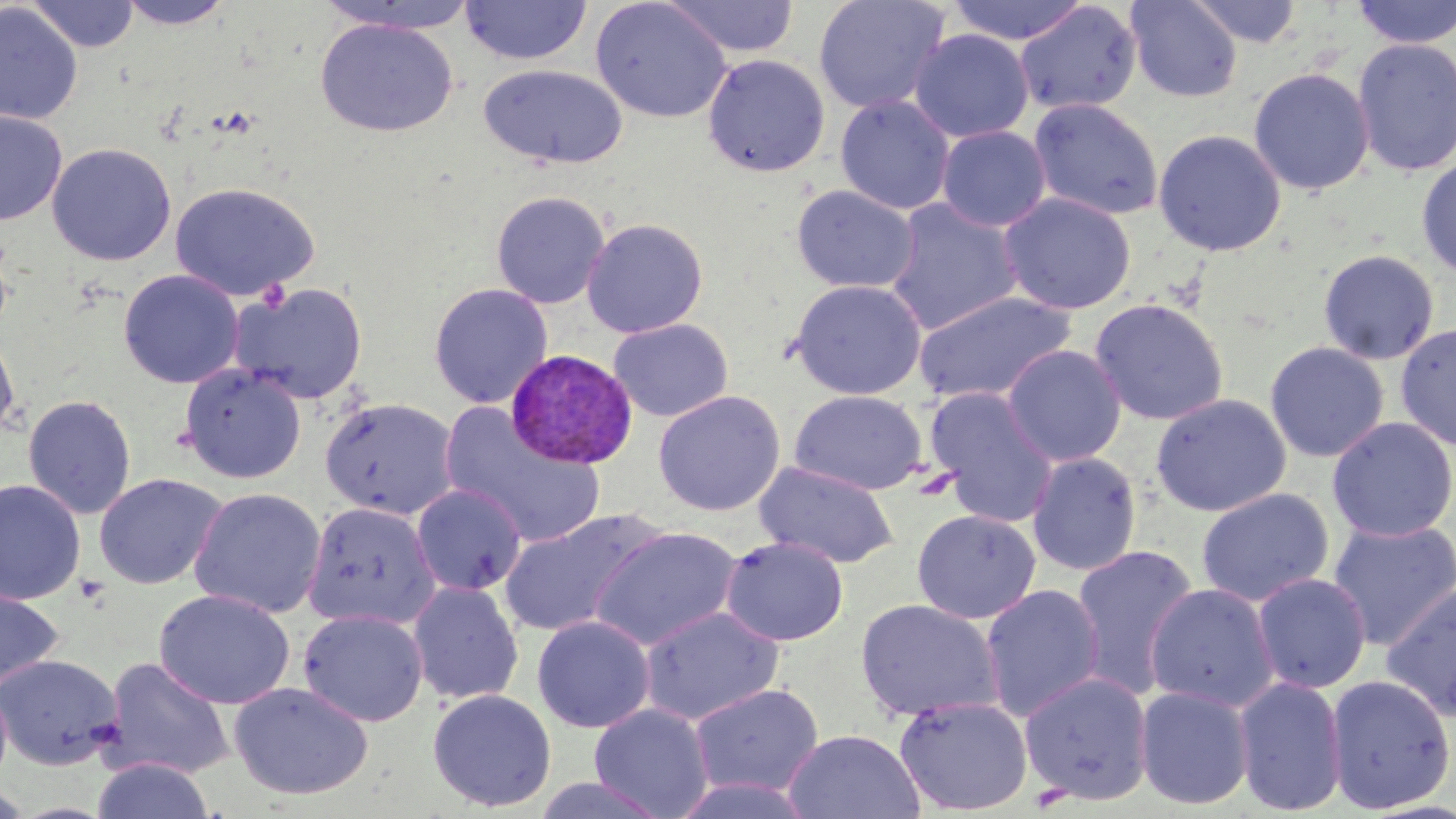
Approximate bounding boxes as (x1, y1, x2, y2) in pixels. Plasmodium vivax-infected red blood cell locations: (505, 347, 639, 470). Uninfected red blood cell locations: (26, 0, 141, 52), (114, 0, 238, 30), (590, 0, 732, 123), (661, 0, 801, 58), (813, 0, 950, 114), (945, 0, 1092, 45), (1125, 0, 1243, 102), (1188, 0, 1303, 48), (1350, 0, 1455, 49), (316, 1, 481, 34), (460, 1, 592, 66), (1014, 2, 1142, 116), (0, 3, 83, 126), (315, 17, 458, 137), (909, 29, 1034, 143), (1352, 38, 1456, 177), (702, 54, 830, 177), (478, 63, 629, 169), (1248, 67, 1375, 196), (835, 95, 955, 214), (1028, 97, 1164, 221), (0, 111, 67, 225), (937, 125, 1051, 232), (1153, 128, 1287, 257), (46, 143, 176, 266), (1416, 155, 1456, 280), (169, 182, 320, 301), (791, 184, 920, 294), (490, 190, 610, 309), (998, 192, 1136, 315), (885, 197, 1024, 336), (581, 217, 709, 338), (1318, 249, 1439, 365), (118, 269, 244, 389), (789, 279, 927, 399), (231, 281, 368, 404), (429, 282, 553, 409), (912, 291, 1076, 405), (1089, 298, 1229, 426), (607, 318, 734, 422), (1395, 322, 1456, 451), (0, 326, 20, 441), (1264, 341, 1389, 463), (1002, 344, 1127, 467), (179, 362, 306, 484), (925, 387, 1059, 528), (652, 390, 786, 517), (789, 390, 927, 495), (1150, 392, 1292, 517), (22, 394, 136, 519), (319, 396, 459, 520), (440, 404, 606, 548), (1327, 416, 1456, 542), (1027, 452, 1141, 576), (755, 461, 898, 568), (94, 472, 227, 590), (0, 479, 86, 605), (411, 483, 527, 596), (189, 487, 327, 618), (1196, 488, 1334, 607), (303, 502, 440, 629), (912, 509, 1041, 624), (498, 511, 660, 637), (1326, 518, 1456, 651), (588, 526, 743, 652), (721, 535, 849, 646), (1070, 543, 1200, 698), (1251, 572, 1372, 693), (407, 581, 524, 705), (1381, 581, 1456, 724), (1144, 582, 1279, 712), (0, 584, 64, 695), (979, 584, 1106, 722), (153, 589, 296, 709), (855, 598, 1003, 723), (639, 605, 785, 726), (298, 608, 429, 727), (532, 615, 656, 733), (0, 654, 125, 769), (100, 657, 235, 781), (1020, 671, 1154, 805), (1325, 674, 1455, 813), (1233, 675, 1347, 815), (228, 681, 374, 800), (689, 683, 824, 798), (1135, 685, 1255, 810), (427, 689, 556, 812), (894, 695, 1033, 815), (589, 703, 714, 819), (783, 729, 925, 818), (91, 757, 216, 819), (531, 775, 670, 819), (670, 775, 819, 818), (0, 783, 34, 818). Slide-level diagnosis: Plasmodium vivax. Light microscopy. One field of a larger specimen. Thin blood film. Image is 1456×819 pixels. May-Grünwald-Giemsa-stained preparation. Captured at 1000x magnification.